Report the malaria status of this cell.
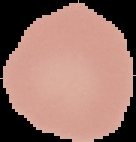

Uninfected.

preparation = thin blood smear
image type = segmented cell region on a black background
image size = 136×142 pixels